Comment on the morphology of the erythrocytes.
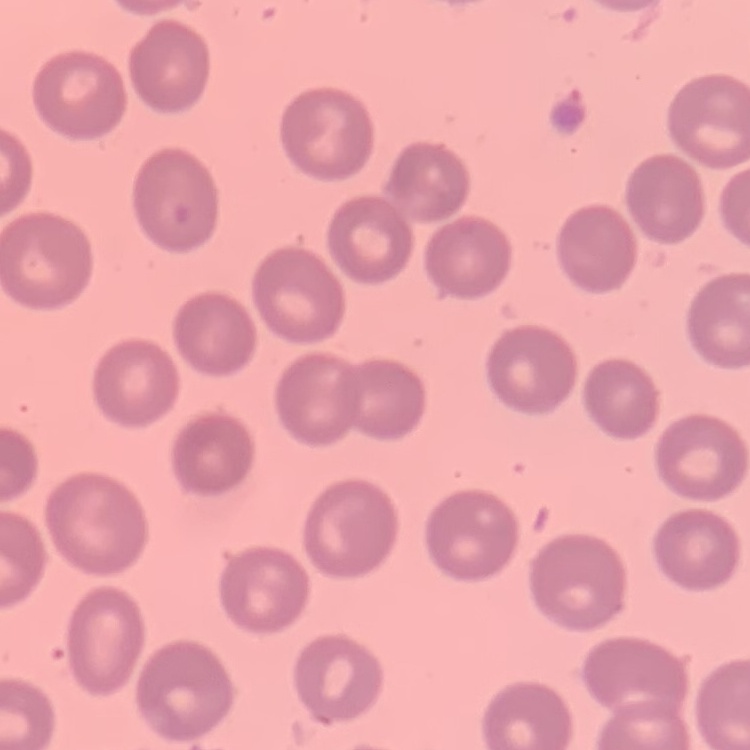

No rouleaux formation.

Stained with either Field's or Giemsa. Thin blood smear. One tile cut from a larger photomicrograph.